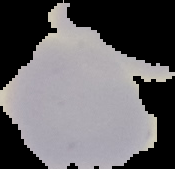

Result: no Plasmodium parasites detected. Segmented cell region on a black background. From a thin blood smear. Image is 175×169 pixels.